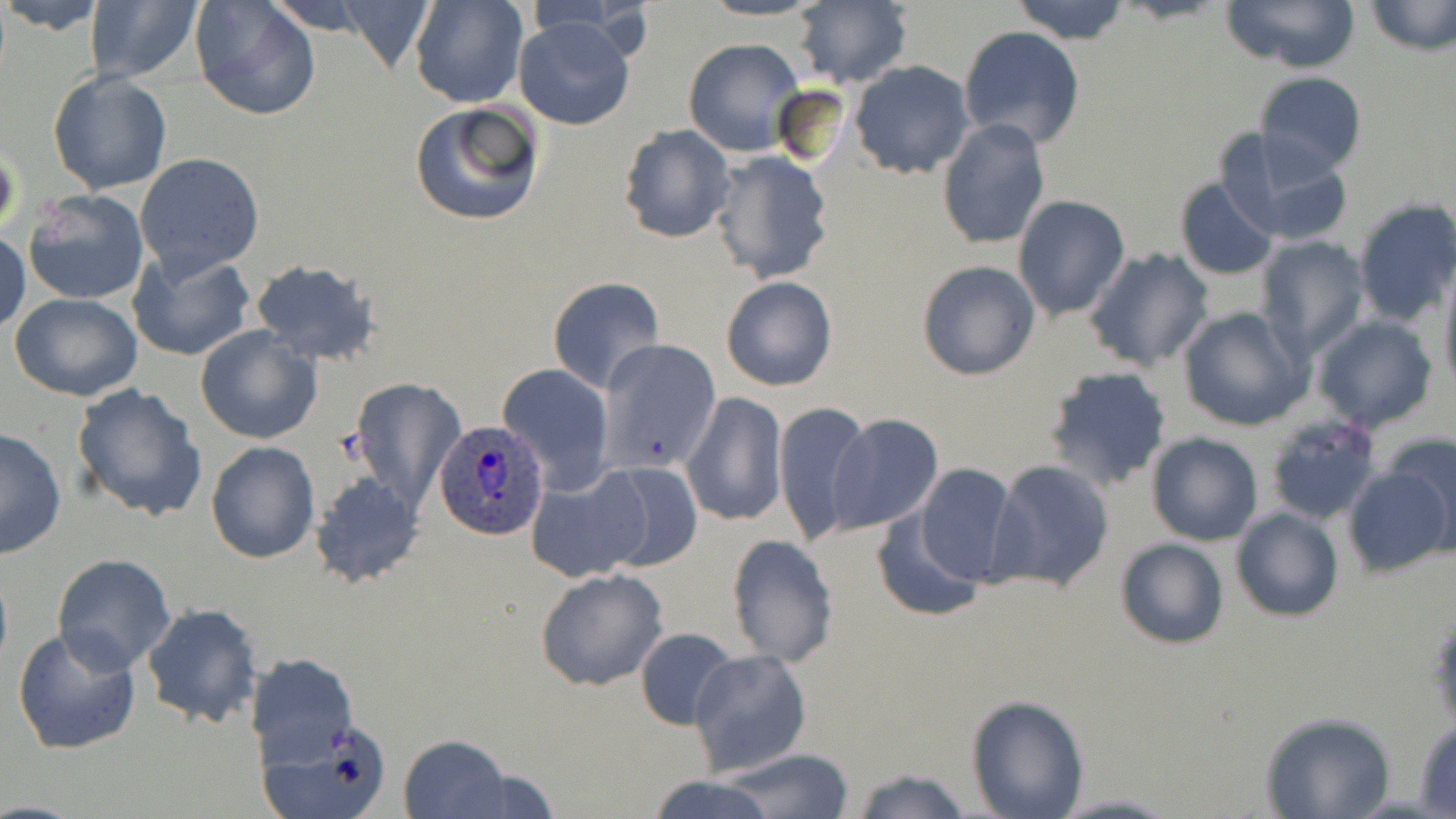
Approximate bounding boxes as (x1,y1)-(x2,y2) corner pairs in pixels. Uninfected red blood cell locations (subset): (2,0)-(102,35), (189,0)-(321,123), (410,0)-(527,108), (697,0)-(825,22), (1011,0)-(1130,43), (1221,0)-(1360,74), (1365,0)-(1456,55), (89,1)-(206,86), (332,1)-(440,73), (790,2)-(913,86), (513,17)-(637,131), (957,26)-(1086,150), (683,37)-(805,157), (847,59)-(976,177), (48,70)-(173,196), (1254,72)-(1367,174), (773,83)-(851,166), (408,100)-(546,229), (938,119)-(1050,250), (618,123)-(737,243), (1215,128)-(1355,247), (0,143)-(19,242), (709,149)-(834,284), (135,153)-(266,279), (1174,178)-(1278,282), (24,189)-(151,307), (1013,195)-(1130,319), (1352,197)-(1456,328), (0,231)-(29,336), (1253,234)-(1372,359), (129,248)-(254,362), (1086,248)-(1213,372), (248,259)-(382,367), (916,260)-(1041,380), (1439,264)-(1456,394), (720,276)-(837,391), (547,278)-(665,392), (10,293)-(143,402), (1176,306)-(1312,432), (1310,315)-(1439,433), (195,327)-(322,444), (595,339)-(721,472), (497,364)-(614,493), (1044,366)-(1172,490), (348,376)-(468,512), (69,382)-(208,522), (683,391)-(787,528), (773,401)-(875,545), (827,413)-(944,533), (1,425)-(66,561), (1380,431)-(1456,552), (1147,432)-(1263,546), (206,442)-(319,564), (986,458)-(1116,593), (593,463)-(703,570), (912,463)-(1020,585), (1344,464)-(1453,578), (525,465)-(651,582), (308,471)-(426,589), (1232,506)-(1343,622), (871,510)-(988,623), (726,533)-(839,667), (1115,538)-(1230,650), (51,554)-(176,673), (0,555)-(12,683), (535,568)-(669,690), (140,602)-(263,729), (1427,603)-(1455,737), (11,625)-(144,757), (636,627)-(739,729), (689,649)-(813,776), (245,652)-(359,766), (966,694)-(1088,818), (1261,712)-(1396,819), (255,716)-(390,819), (1413,717)-(1456,815), (398,732)-(513,818), (718,747)-(856,819), (453,764)-(561,817), (851,766)-(973,819), (641,776)-(782,819), (1052,793)-(1178,818). Plasmodium ovale-infected red blood cell locations (subset): (435,419)-(550,539). Slide-level diagnosis: Plasmodium ovale. Optical microscopy. May-Grünwald-Giemsa stain. 1000x magnification. One field of a larger specimen. Thin blood smear. Image is 1456×819 pixels.